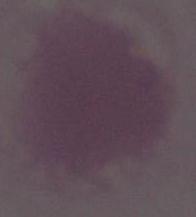
identification = red blood cell
magnification = 1000x
modality = photomicrograph